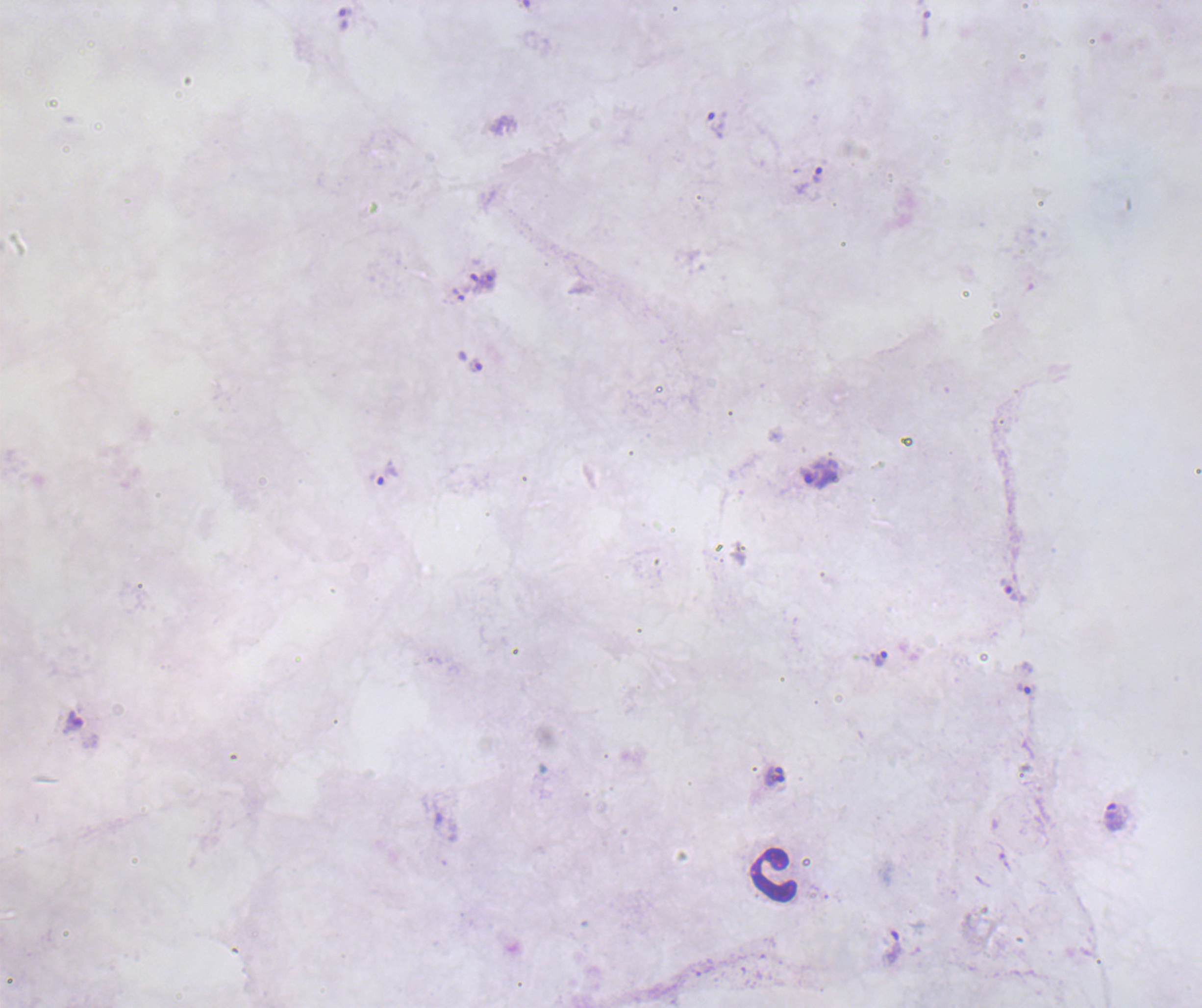
Approximate object centers, in pixels from the top-left corner. Trophozoite locations: (x=716, y=125), (x=809, y=179), (x=488, y=279), (x=475, y=365), (x=817, y=471), (x=384, y=472), (x=1009, y=591), (x=879, y=659), (x=1026, y=688), (x=775, y=770), (x=775, y=780), (x=1113, y=817), (x=891, y=947). Leukocyte locations: (x=774, y=875). One field from this slide. Thick smear of blood. Romanowsky stain. Captured at 100x magnification. Previously used in an actual diagnosis. Background quality: poor. Coloration quality: bad. Result: Plasmodium parasites identified. Image is 1202×1008 pixels.